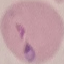

result: malaria parasites detected
image_type: automatically extracted cell patch, resized to 64 × 64 pixels
stain: Giemsa
capture: smartphone camera at the microscope eyepiece
preparation: thin blood smear